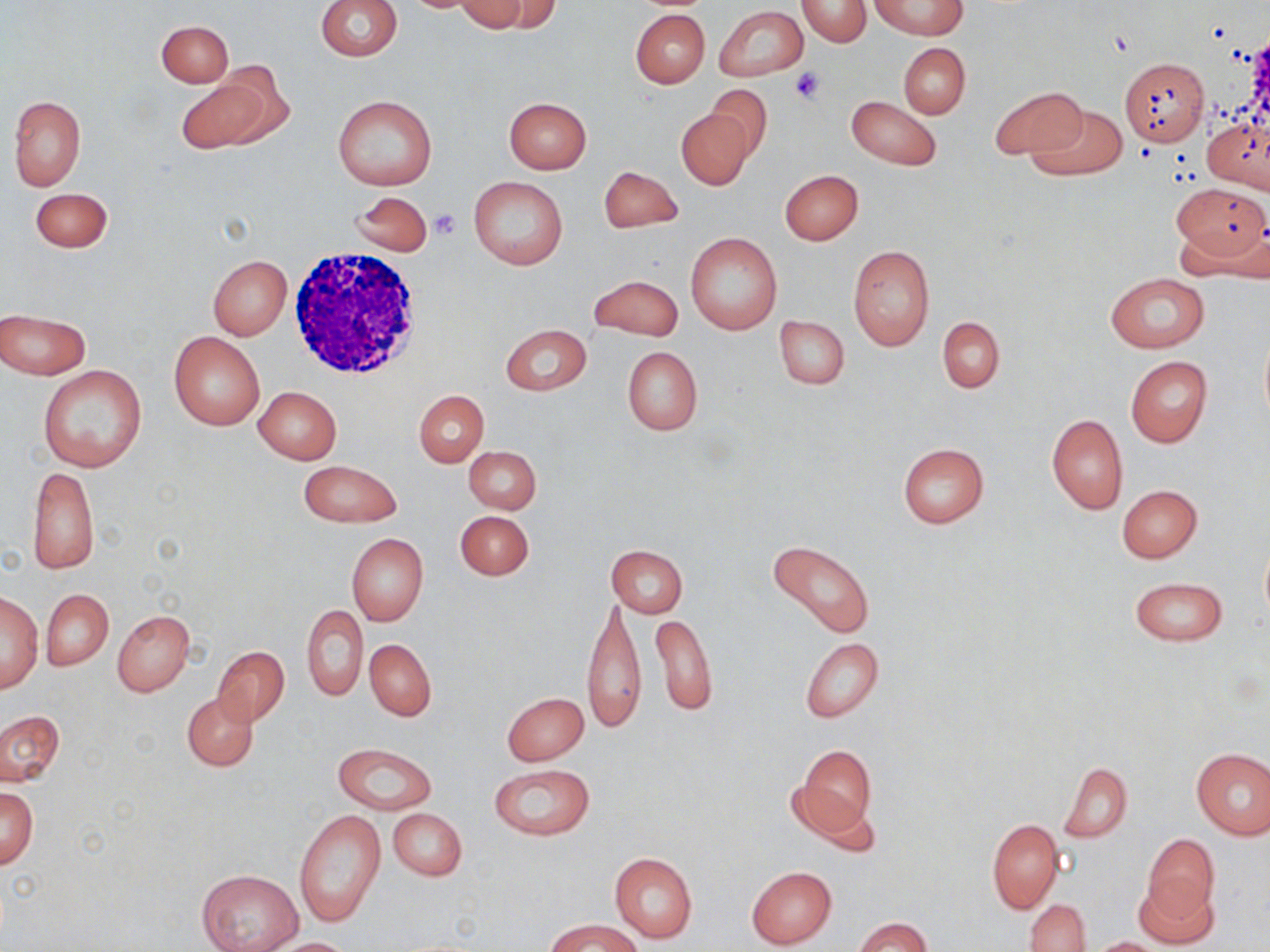
Summary:
  - Coordinate format: approximate bounding boxes as (x1,y1)-(x2,y2) corner pairs in pixels
  - Platelet locations: (788,66)-(828,104), (430,209)-(462,239)
  - White blood cell locations: (286,247)-(430,383)
  - Uninfected red blood cell locations: (315,0)-(402,60), (473,0)-(561,37), (870,0)-(966,38), (797,1)-(871,47), (454,2)-(529,33), (715,5)-(807,82), (630,10)-(709,88), (156,20)-(232,86), (898,43)-(970,119), (1120,56)-(1209,145), (175,72)-(279,153), (704,86)-(773,162), (990,88)-(1088,160), (332,95)-(437,190), (846,95)-(941,170), (8,96)-(86,190), (503,96)-(592,173), (1026,102)-(1126,180), (677,107)-(754,190), (1204,114)-(1269,193), (597,166)-(683,233), (780,170)-(863,245), (468,175)-(568,269), (1172,186)-(1267,267), (29,187)-(113,252), (350,191)-(433,256), (685,232)-(782,335), (847,244)-(936,350), (208,255)-(292,340), (1106,273)-(1207,353), (587,275)-(684,341), (1,308)-(91,379), (775,316)-(850,390), (937,317)-(1005,392), (499,323)-(592,396), (1258,330)-(1270,427), (169,331)-(265,430), (622,347)-(702,435), (1125,356)-(1212,448), (37,365)-(147,473), (254,386)-(342,464), (415,390)-(488,467), (1047,414)-(1127,514), (896,441)-(990,529), (464,446)-(542,513), (298,459)-(402,528), (27,464)-(99,575), (1117,484)-(1202,563), (455,509)-(535,581), (346,532)-(428,627), (765,539)-(875,640), (1260,541)-(1270,631), (606,544)-(688,617), (1128,576)-(1228,648), (41,590)-(113,670), (1,593)-(42,692), (581,598)-(647,734), (301,606)-(367,701), (113,610)-(193,697), (650,612)-(717,716), (800,638)-(885,723), (365,639)-(437,721), (213,645)-(290,725), (502,692)-(588,766), (182,693)-(258,770), (0,710)-(64,787), (333,743)-(437,814), (793,744)-(876,839), (1191,748)-(1270,840), (1061,762)-(1133,842), (489,764)-(596,840), (1,788)-(38,869), (293,807)-(387,928), (388,808)-(467,882), (987,818)-(1063,913), (1141,833)-(1219,929), (609,852)-(698,944), (747,866)-(837,949), (196,869)-(303,952), (1133,875)-(1221,951), (1026,898)-(1089,951), (855,916)-(930,951), (549,919)-(641,952), (267,937)-(357,951), (1088,937)-(1170,951)
  - Slide-level diagnosis: negative for blood parasites
  - Magnification: 1000x
  - Stain: May-Grünwald-Giemsa
  - Field of view: one of a larger specimen
  - Preparation: thin blood film
  - Image size: 1270×952 pixels
  - Modality: optical microscopy